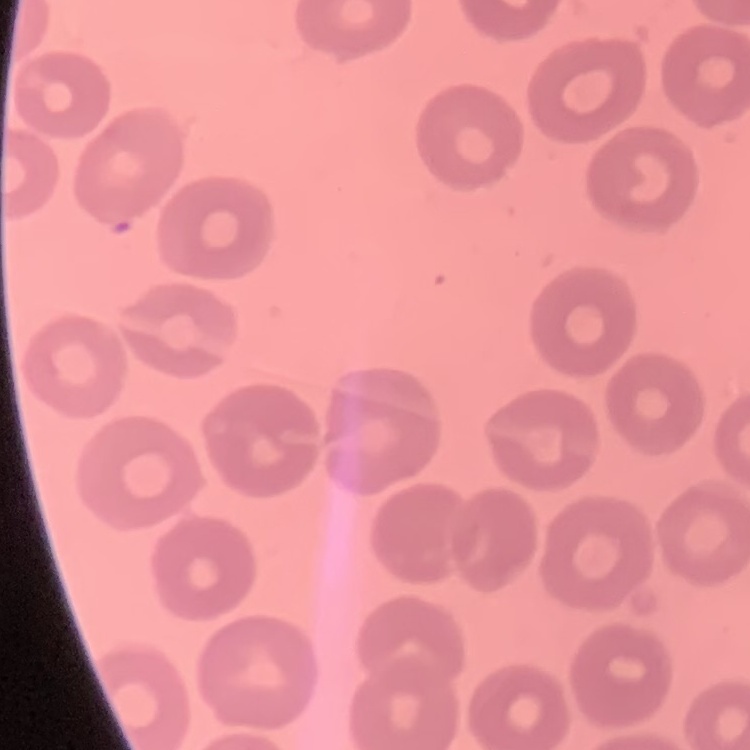

Summary:
  - Red blood cell morphology: no rouleaux formation
  - Preparation: thin blood smear
  - Image type: square crop of a larger photomicrograph
  - Stain: Field's or Giemsa